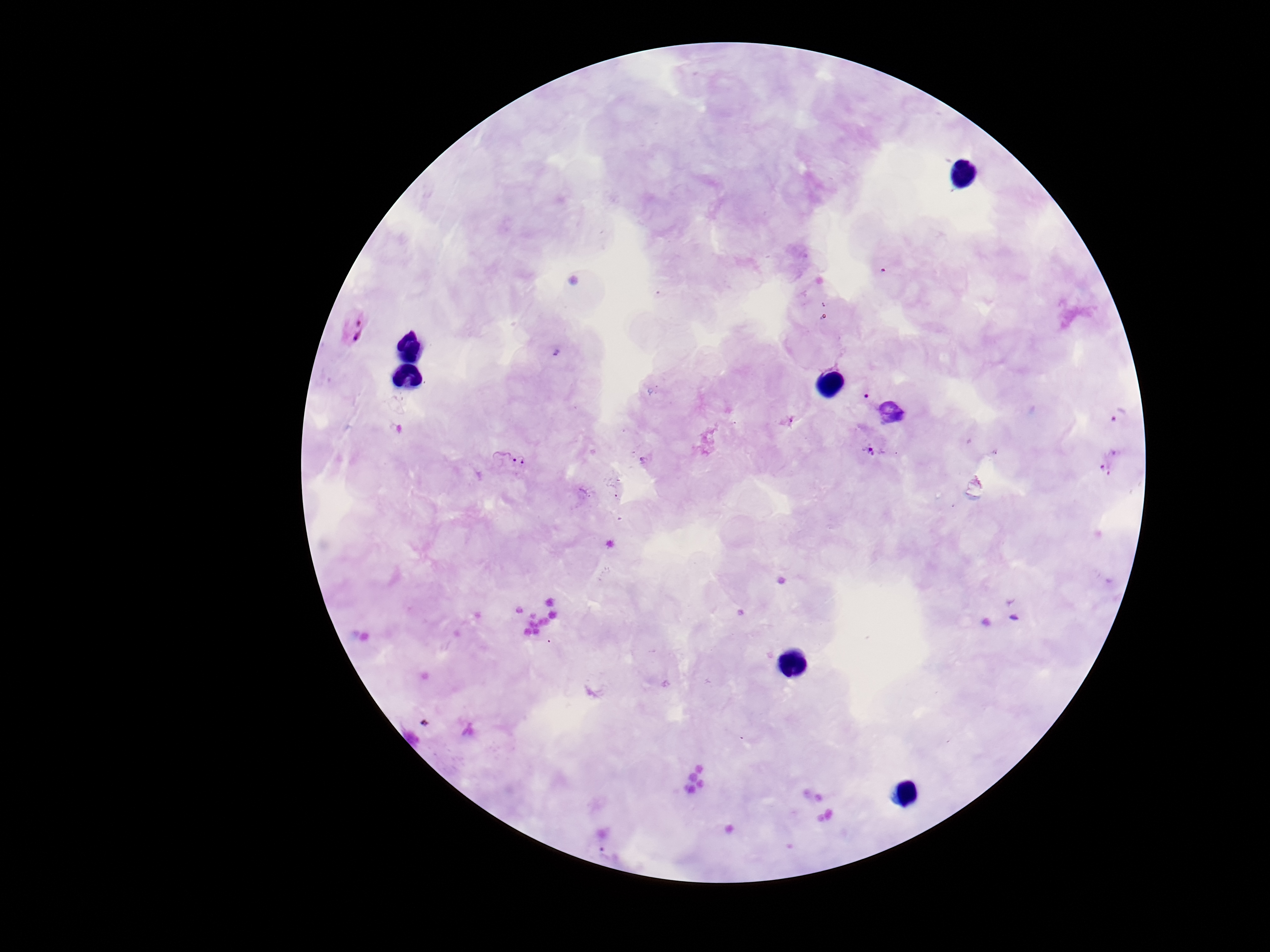

{
  "patient_malaria_status": "infected",
  "preparation": "thick blood film",
  "image_size": "1270×952 pixels",
  "capture": "smartphone camera through the microscope eyepiece",
  "magnification": "100x",
  "field_of_view": "single",
  "stain": "Giemsa",
  "plasmodium_parasite_locations": "approximate centers as {x, y} in pixels: {354, 326}, {789, 421}, {870, 450}, {508, 463}"
}